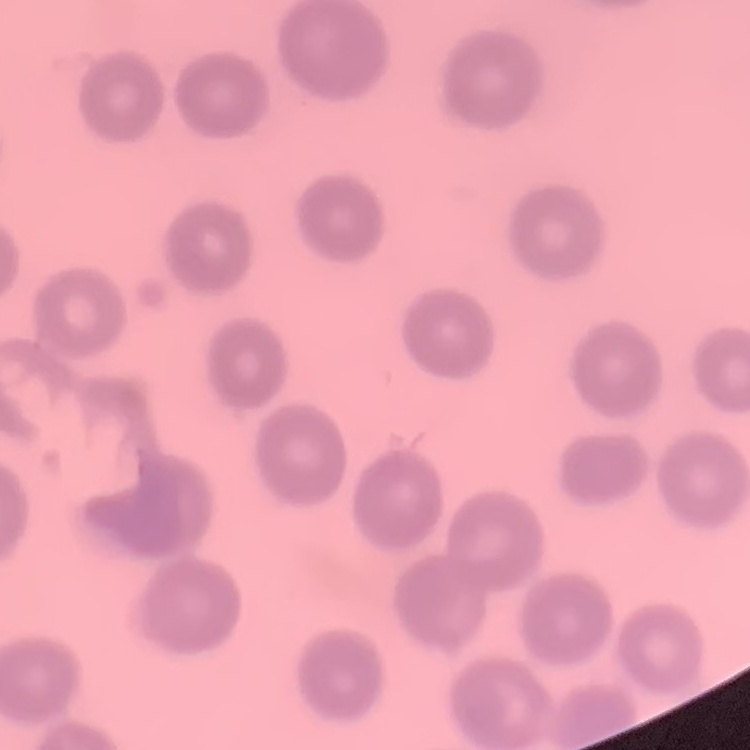

The red blood cells exhibit no rouleaux formation. Thin peripheral smear. Field's or Giemsa stain. One tile cut from a larger photomicrograph.